Assess this cell for malaria.
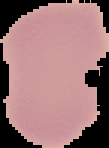

Uninfected.

image size = 109×148 pixels
image type = segmented cell region on a black background
preparation = thin blood film